Locate every blood parasite and identify its species.
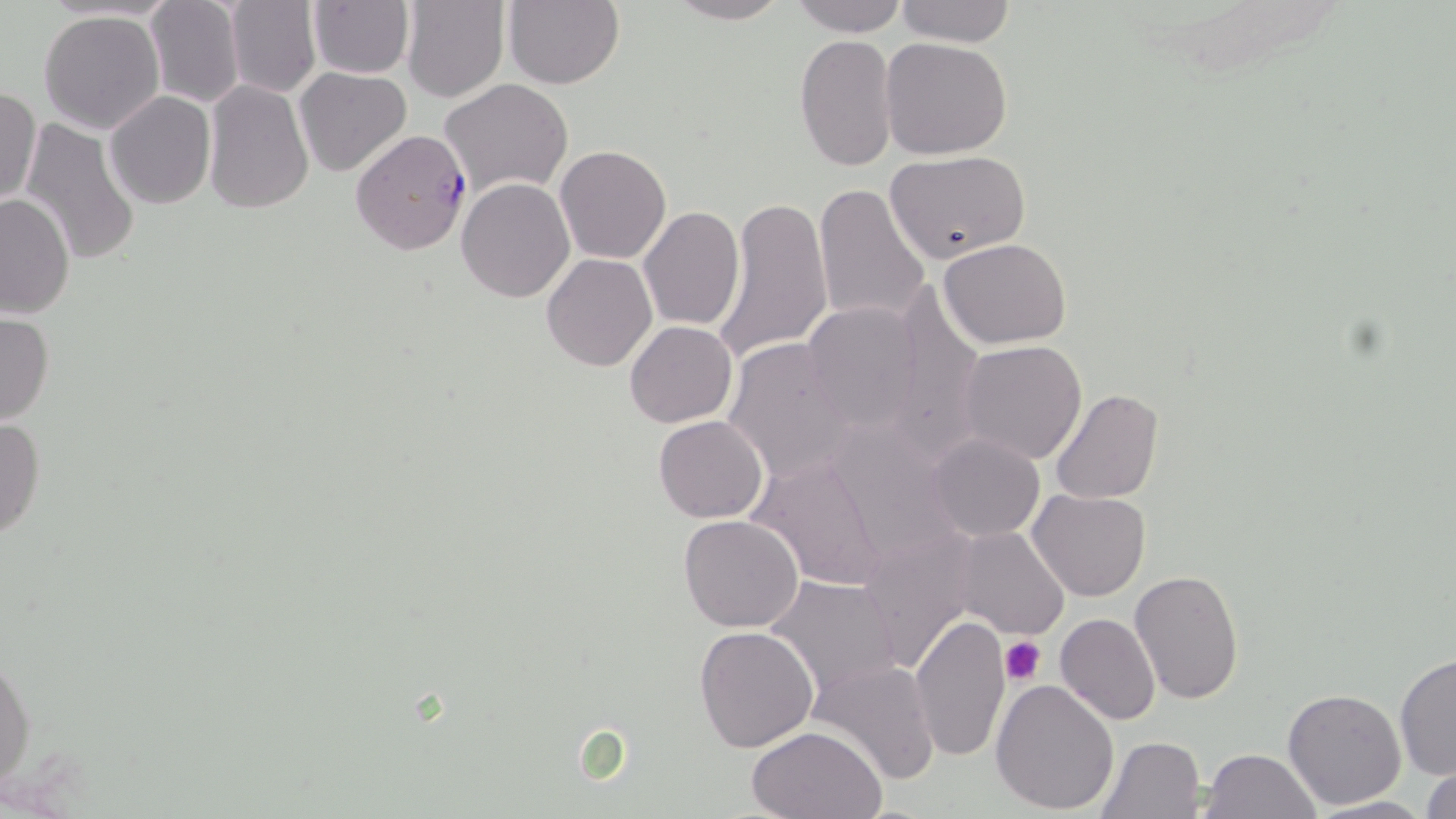

Approximate bounding boxes as (x1,y1)-(x2,y2) corner pairs in pixels.
Plasmodium falciparum-infected red blood cells: (351,128)-(472,256).
No Plasmodium ovale, Plasmodium malariae, Plasmodium vivax, Babesia divergens, or Trypanosoma brucei observed.

Platelet locations: (1001,637)-(1045,686). Uninfected red blood cell locations: (143,0)-(245,108), (223,0)-(321,99), (400,0)-(509,102), (502,0)-(626,89), (663,0)-(790,25), (894,0)-(1018,47), (307,1)-(414,79), (787,1)-(909,37), (39,9)-(165,134), (793,35)-(899,174), (880,36)-(1014,159), (295,68)-(413,178), (203,78)-(314,214), (439,78)-(574,199), (1,87)-(41,206), (104,92)-(216,209), (21,119)-(144,268), (554,144)-(671,264), (884,149)-(1030,263), (456,178)-(574,302), (813,181)-(930,328), (0,191)-(77,319), (714,195)-(833,363), (638,205)-(745,330), (939,238)-(1072,349), (541,254)-(657,372), (884,284)-(986,462), (800,301)-(924,433), (0,312)-(54,425), (625,320)-(737,428), (722,337)-(860,484), (958,339)-(1089,465), (1049,388)-(1164,503), (0,415)-(46,542), (653,415)-(769,524), (925,433)-(1046,542), (946,450)-(1088,566), (751,455)-(891,592), (1028,489)-(1149,602), (678,514)-(805,632), (954,526)-(1069,640), (855,527)-(980,674), (1129,569)-(1247,705), (765,574)-(905,701), (1055,611)-(1160,725), (912,614)-(1011,762), (695,626)-(820,750), (1,645)-(35,791), (1393,652)-(1455,780), (809,659)-(942,785), (990,677)-(1120,814), (1281,688)-(1407,811), (745,726)-(887,818), (1097,735)-(1207,817), (1199,748)-(1320,819), (1418,758)-(1456,818), (1303,795)-(1438,817). Slide-level diagnosis: Plasmodium falciparum. Thin blood film. May-Grünwald-Giemsa stain. Image is 1456×819 pixels. Light microscopy. One field of a larger specimen. Captured at 1000x magnification.